Identify the parasite.
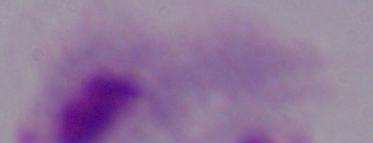
A trichomonad.

1000x magnification. Micrograph.